State the blood parasite species.
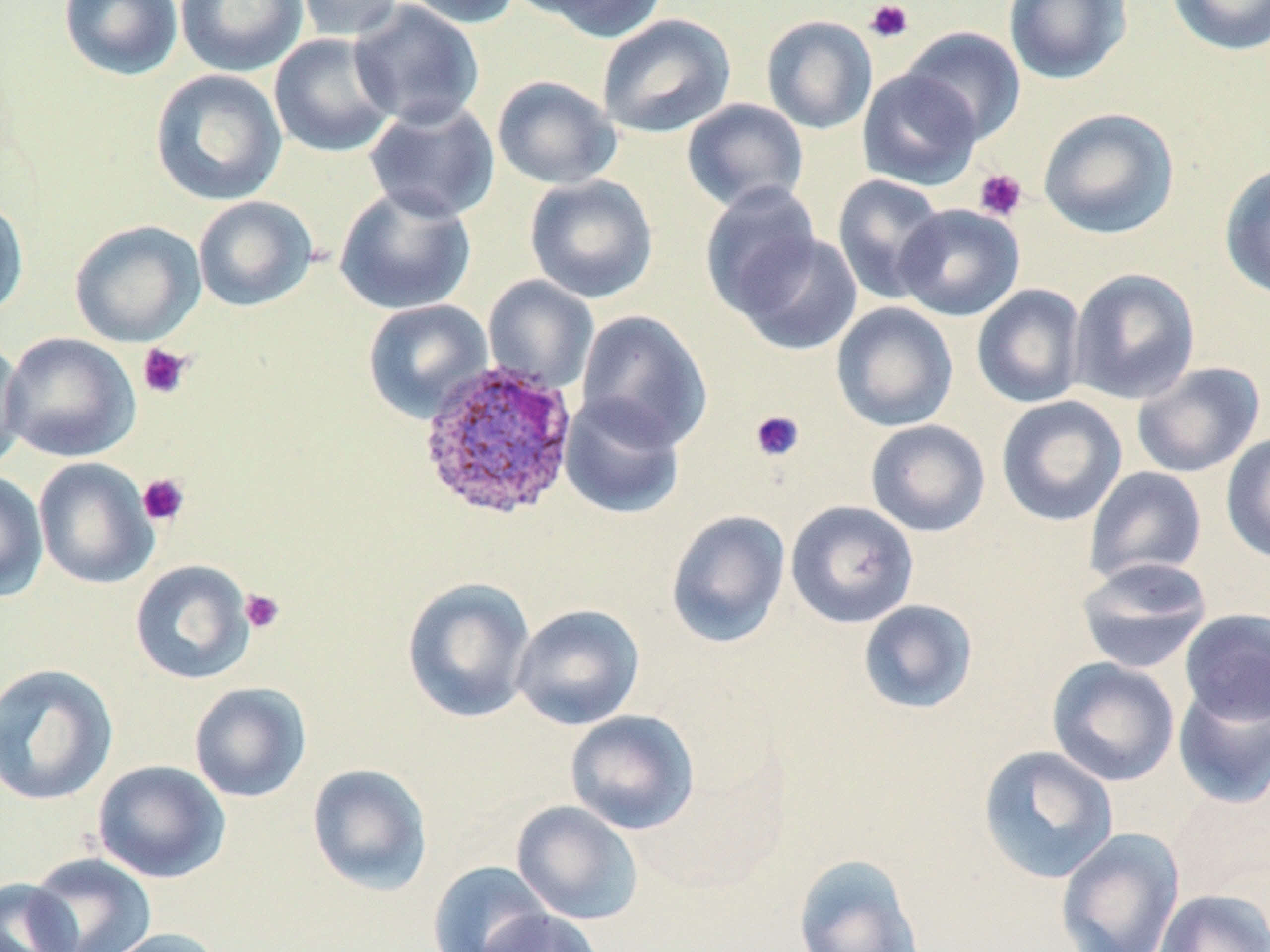

Plasmodium ovale.

Approximate bounding boxes as named x1/y1/x2/y2 corners in pixels. Uninfected red blood cell locations: (x1=59, y1=0, x2=184, y2=81), (x1=175, y1=0, x2=308, y2=77), (x1=292, y1=0, x2=405, y2=43), (x1=397, y1=0, x2=523, y2=29), (x1=517, y1=0, x2=669, y2=41), (x1=1003, y1=0, x2=1132, y2=86), (x1=1166, y1=0, x2=1270, y2=56), (x1=348, y1=1, x2=485, y2=130), (x1=596, y1=14, x2=736, y2=139), (x1=761, y1=15, x2=878, y2=135), (x1=900, y1=25, x2=1027, y2=144), (x1=268, y1=33, x2=398, y2=158), (x1=857, y1=68, x2=983, y2=191), (x1=150, y1=69, x2=288, y2=206), (x1=492, y1=75, x2=621, y2=190), (x1=362, y1=98, x2=500, y2=224), (x1=681, y1=98, x2=809, y2=213), (x1=1037, y1=107, x2=1180, y2=239), (x1=1219, y1=162, x2=1270, y2=302), (x1=524, y1=174, x2=658, y2=303), (x1=831, y1=174, x2=948, y2=304), (x1=700, y1=182, x2=822, y2=317), (x1=334, y1=185, x2=477, y2=316), (x1=0, y1=196, x2=29, y2=320), (x1=193, y1=196, x2=317, y2=312), (x1=894, y1=203, x2=1025, y2=322), (x1=69, y1=220, x2=206, y2=347), (x1=732, y1=231, x2=863, y2=356), (x1=1068, y1=268, x2=1200, y2=405), (x1=483, y1=275, x2=599, y2=394), (x1=971, y1=284, x2=1087, y2=408), (x1=362, y1=299, x2=494, y2=423), (x1=831, y1=302, x2=959, y2=432), (x1=576, y1=309, x2=713, y2=451), (x1=1, y1=332, x2=141, y2=463), (x1=0, y1=336, x2=27, y2=475), (x1=1131, y1=361, x2=1265, y2=478), (x1=558, y1=393, x2=686, y2=520), (x1=995, y1=394, x2=1128, y2=527), (x1=865, y1=419, x2=990, y2=537), (x1=1221, y1=431, x2=1270, y2=565), (x1=33, y1=457, x2=159, y2=589), (x1=1083, y1=466, x2=1208, y2=585), (x1=0, y1=470, x2=49, y2=602), (x1=785, y1=500, x2=920, y2=628), (x1=665, y1=509, x2=791, y2=649), (x1=1076, y1=556, x2=1213, y2=674), (x1=129, y1=559, x2=256, y2=685), (x1=401, y1=576, x2=537, y2=724), (x1=857, y1=599, x2=979, y2=714), (x1=511, y1=603, x2=645, y2=730), (x1=1179, y1=609, x2=1270, y2=726), (x1=1046, y1=657, x2=1181, y2=787), (x1=0, y1=662, x2=119, y2=806), (x1=189, y1=682, x2=312, y2=803), (x1=1172, y1=682, x2=1270, y2=808), (x1=564, y1=710, x2=701, y2=835), (x1=978, y1=745, x2=1119, y2=884), (x1=92, y1=759, x2=231, y2=883), (x1=306, y1=763, x2=433, y2=895), (x1=1167, y1=783, x2=1270, y2=906), (x1=511, y1=800, x2=644, y2=925), (x1=1054, y1=828, x2=1185, y2=952), (x1=25, y1=852, x2=157, y2=952), (x1=793, y1=853, x2=925, y2=952), (x1=427, y1=860, x2=553, y2=952), (x1=0, y1=877, x2=80, y2=952), (x1=1154, y1=888, x2=1270, y2=952), (x1=477, y1=907, x2=604, y2=952), (x1=95, y1=927, x2=228, y2=952). Platelet locations: (x1=864, y1=1, x2=914, y2=43), (x1=974, y1=168, x2=1027, y2=221), (x1=137, y1=343, x2=193, y2=399), (x1=749, y1=409, x2=804, y2=462), (x1=137, y1=473, x2=190, y2=527), (x1=239, y1=588, x2=285, y2=634). Plasmodium ovale-infected red blood cell locations: (x1=416, y1=359, x2=579, y2=522). May-Grünwald-Giemsa-stained preparation. Captured at 1000x magnification. One field of a larger specimen. Light microscopy. Thin blood film. Image is 1270×952 pixels.